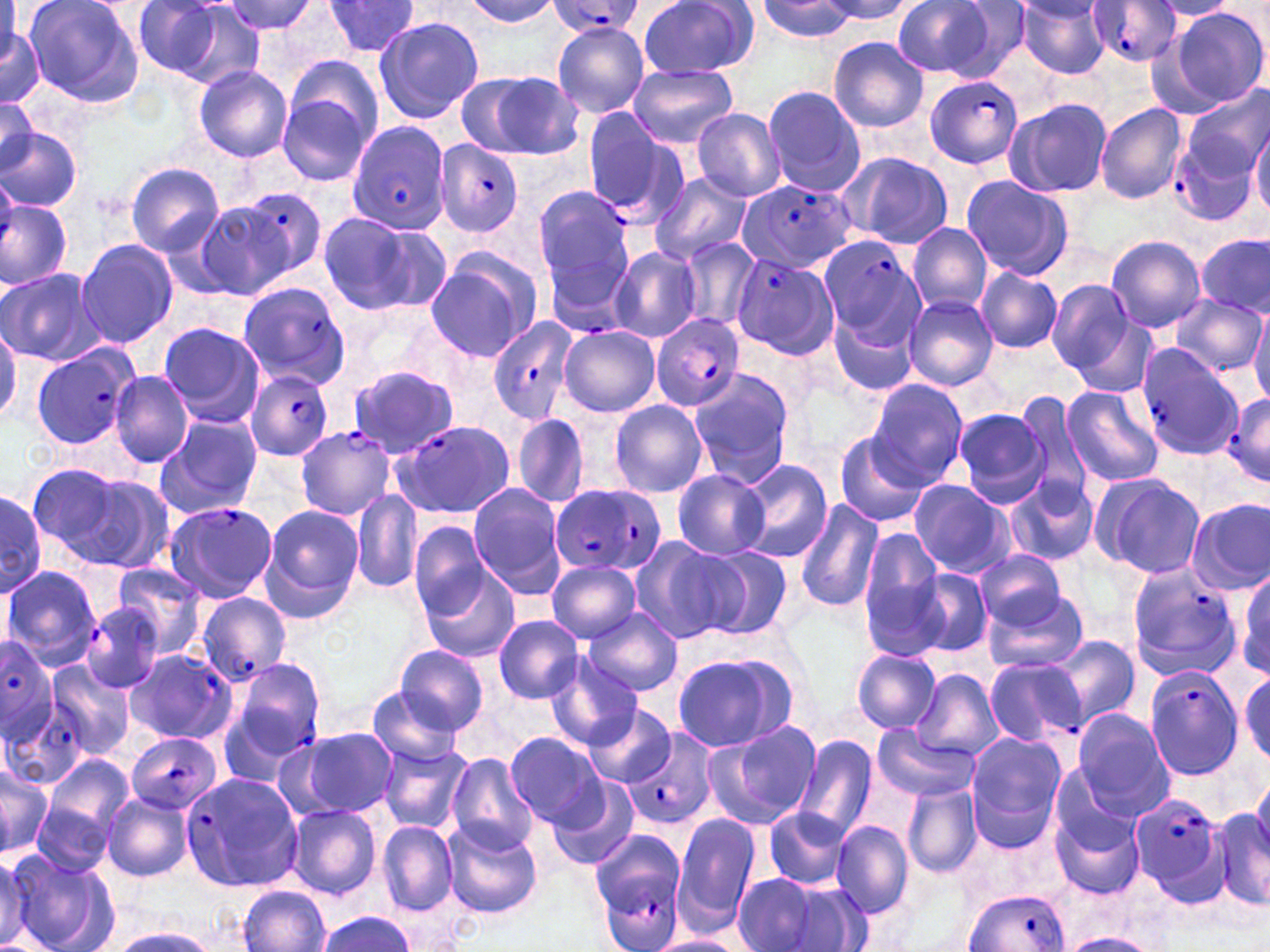
slide-level diagnosis = Plasmodium falciparum
image size = 1270×952 pixels
preparation = thin blood smear
uninfected red blood cell locations = approximate bounding boxes as [x1, y1, x2, y2] in pixels: [22, 0, 143, 107], [129, 0, 239, 79], [218, 0, 322, 40], [636, 0, 757, 80], [891, 0, 996, 78], [944, 0, 1034, 80], [1016, 0, 1111, 79], [322, 1, 421, 58], [463, 1, 562, 25], [756, 1, 859, 41], [817, 1, 916, 24], [1151, 1, 1238, 22], [1170, 7, 1267, 106], [373, 15, 483, 125], [2, 21, 42, 106], [552, 24, 650, 117], [828, 36, 927, 132], [286, 56, 387, 155], [193, 64, 292, 162], [628, 64, 737, 147], [465, 70, 584, 160], [762, 85, 866, 197], [1181, 87, 1270, 181], [277, 94, 372, 186], [0, 97, 39, 175], [1004, 98, 1112, 198], [1094, 103, 1187, 204], [690, 107, 786, 200], [1250, 117, 1270, 216], [0, 127, 81, 211], [837, 151, 955, 249], [125, 163, 224, 256], [650, 172, 754, 266], [960, 176, 1075, 279], [533, 185, 633, 290], [192, 201, 295, 300], [315, 212, 437, 317], [908, 223, 991, 316], [1105, 235, 1206, 332], [1198, 235, 1268, 316], [74, 237, 178, 348], [677, 239, 759, 334], [607, 247, 702, 343], [424, 250, 542, 362], [976, 267, 1061, 353], [0, 268, 100, 365], [1048, 280, 1136, 375], [1171, 294, 1265, 376], [902, 295, 996, 389], [828, 307, 920, 396], [1061, 308, 1158, 396], [1250, 308, 1270, 406], [0, 319, 20, 425], [157, 320, 264, 426], [559, 326, 660, 417], [348, 365, 459, 457], [688, 368, 795, 487], [109, 371, 194, 468], [867, 379, 969, 486], [1060, 386, 1164, 486], [1014, 392, 1093, 503], [609, 399, 708, 499], [953, 408, 1050, 508], [512, 411, 590, 511], [153, 415, 261, 520], [834, 431, 929, 529], [735, 458, 832, 562], [23, 463, 140, 565], [673, 470, 770, 560], [78, 473, 178, 575], [1005, 474, 1098, 567], [1093, 474, 1206, 578], [908, 480, 1016, 579], [467, 483, 567, 595], [0, 487, 47, 597], [351, 489, 423, 596], [795, 499, 883, 613], [1188, 500, 1269, 594], [259, 504, 363, 618], [408, 520, 492, 617], [857, 531, 948, 646], [629, 539, 735, 646], [693, 545, 794, 639], [978, 551, 1068, 631], [419, 561, 520, 662], [546, 561, 642, 643], [108, 563, 210, 660], [2, 566, 102, 670], [912, 567, 992, 658], [1236, 567, 1268, 678], [985, 590, 1089, 676], [585, 607, 683, 697], [494, 615, 582, 703], [1046, 634, 1140, 729], [394, 644, 488, 734], [851, 648, 943, 733], [672, 651, 800, 752], [547, 654, 642, 751], [44, 662, 133, 761], [913, 670, 1002, 762], [1239, 670, 1270, 765], [367, 688, 466, 766], [587, 704, 676, 786], [1070, 708, 1173, 813], [707, 720, 823, 829], [282, 727, 400, 820], [873, 727, 976, 799], [505, 731, 605, 829], [964, 731, 1065, 842], [793, 733, 879, 840], [379, 744, 470, 832], [446, 754, 538, 853], [44, 755, 134, 844], [0, 759, 52, 858], [1045, 763, 1145, 857], [1252, 774, 1270, 854], [548, 779, 639, 870], [903, 783, 983, 877], [103, 792, 193, 882], [33, 799, 113, 876], [285, 803, 381, 898], [1213, 807, 1270, 913], [761, 808, 852, 888], [671, 815, 760, 931], [1054, 816, 1144, 898], [441, 820, 542, 919], [832, 820, 912, 918], [378, 821, 458, 915], [0, 854, 34, 949], [8, 854, 118, 952], [732, 873, 825, 950], [779, 880, 877, 951], [238, 885, 330, 952], [316, 912, 418, 951], [109, 923, 219, 951], [1063, 933, 1158, 952], [649, 934, 744, 952]
magnification = 1000x
field of view = single
stain = May-Grünwald-Giemsa
modality = optical microscopy
Plasmodium falciparum-infected red blood cell locations = approximate bounding boxes as [x1, y1, x2, y2] in pixels: [1089, 1, 1183, 68], [544, 2, 649, 38], [922, 74, 1023, 168], [583, 111, 683, 222], [345, 119, 449, 232], [1171, 133, 1262, 226], [431, 140, 526, 240], [738, 179, 856, 272], [238, 186, 327, 279], [0, 198, 71, 288], [815, 234, 921, 342], [731, 253, 841, 360], [548, 259, 640, 340], [237, 281, 352, 390], [650, 312, 746, 411], [488, 317, 578, 425], [29, 343, 142, 449], [1135, 345, 1244, 459], [245, 371, 334, 461], [1223, 393, 1270, 484], [393, 419, 515, 519], [294, 425, 395, 520], [551, 484, 666, 577], [162, 502, 277, 604], [1127, 562, 1241, 681], [197, 593, 292, 685], [80, 600, 167, 693], [0, 636, 59, 741], [123, 650, 236, 744], [227, 657, 324, 766], [984, 657, 1084, 747], [1144, 666, 1245, 780], [3, 698, 89, 790], [621, 726, 719, 833], [126, 731, 222, 815], [180, 772, 302, 894], [1127, 793, 1227, 900], [591, 836, 688, 951], [965, 889, 1073, 952]